Outline each uninfected red blood cell.
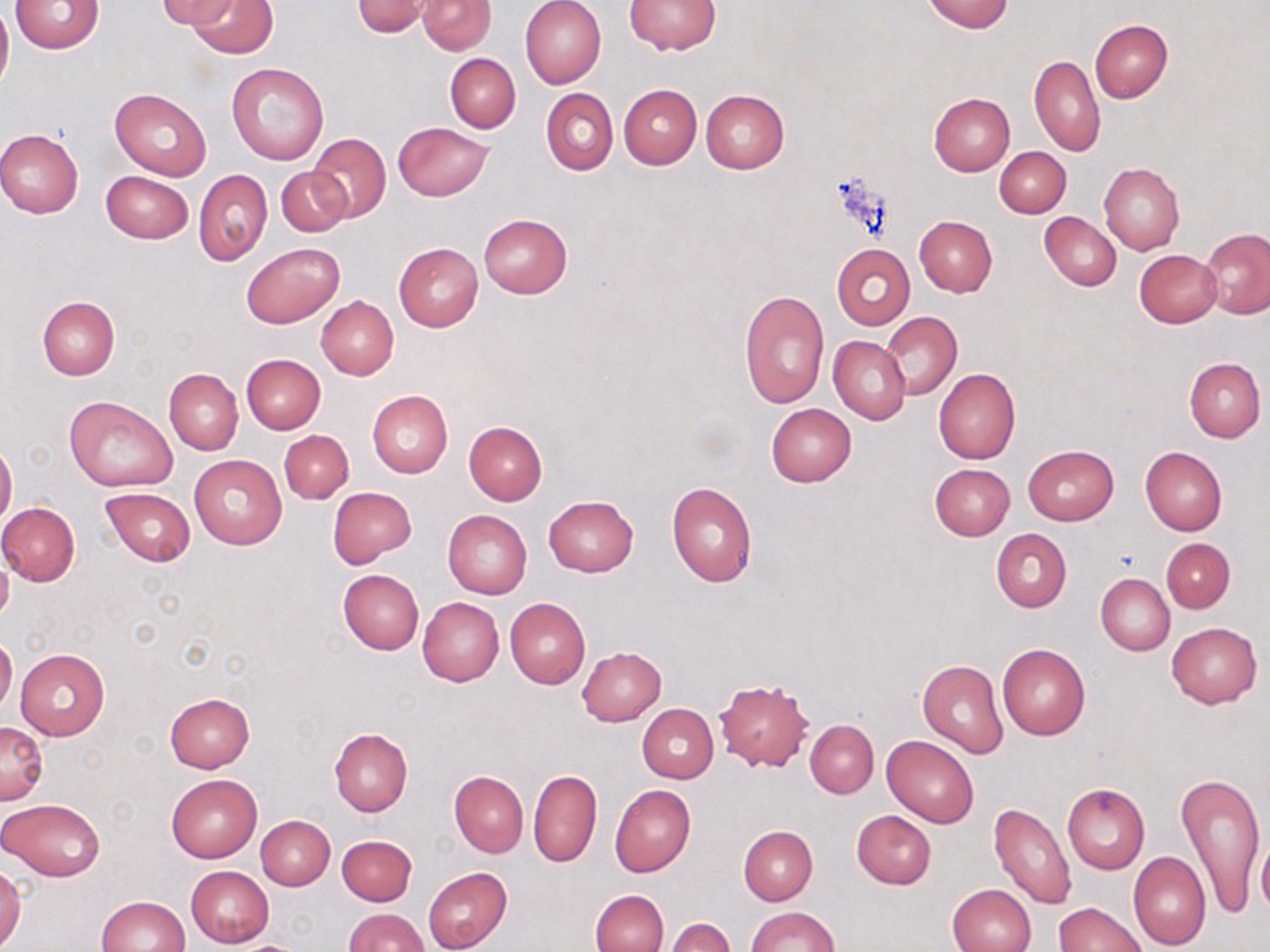
Approximate bounding boxes as (x1,y1)-(x2,y2) corner pairs in pixels.
Uninfected red blood cells: (10,0)-(103,53), (158,0)-(238,29), (188,0)-(278,58), (418,0)-(494,54), (519,0)-(606,89), (922,0)-(1014,33), (0,1)-(13,94), (352,1)-(433,37), (626,1)-(720,54), (1089,19)-(1172,102), (445,53)-(520,132), (1029,55)-(1105,157), (226,62)-(330,165), (619,83)-(701,169), (541,87)-(618,175), (110,88)-(210,180), (701,89)-(789,174), (929,92)-(1015,176), (393,122)-(493,201), (0,130)-(83,219), (306,132)-(391,223), (995,147)-(1070,218), (1099,163)-(1184,254), (277,168)-(349,237), (100,170)-(194,244), (194,170)-(272,264), (1039,212)-(1122,291), (479,213)-(571,297), (915,216)-(996,297), (1201,228)-(1270,318), (242,242)-(344,328), (393,243)-(484,332), (832,244)-(915,328), (1134,250)-(1221,328), (738,289)-(830,410), (317,296)-(398,380), (36,297)-(119,380), (882,310)-(962,401), (828,336)-(911,423), (242,354)-(325,434), (1184,358)-(1265,443), (933,368)-(1020,465), (164,369)-(242,454), (367,390)-(453,477), (65,395)-(177,490), (766,403)-(856,486), (464,422)-(546,504), (279,430)-(353,503), (0,440)-(17,528), (1022,444)-(1119,526), (1140,447)-(1227,536), (189,455)-(286,549), (930,464)-(1014,540), (667,482)-(757,586), (327,486)-(415,566), (101,487)-(195,566), (544,496)-(638,577), (0,502)-(81,585), (443,509)-(532,600), (991,528)-(1072,612), (1162,538)-(1234,613), (0,550)-(13,627), (337,569)-(424,655), (1095,573)-(1175,655), (417,596)-(505,686), (505,597)-(590,689), (1166,622)-(1262,708), (0,636)-(17,713), (997,644)-(1091,740), (577,646)-(666,725), (15,649)-(109,739), (917,659)-(1007,758), (715,680)-(813,771), (164,692)-(254,771), (637,703)-(719,783), (805,719)-(878,798), (0,722)-(48,804), (329,728)-(413,816), (882,735)-(979,828), (528,768)-(601,868), (450,770)-(527,856), (1176,770)-(1266,918), (166,774)-(263,862), (1062,783)-(1149,873), (610,784)-(695,876), (1,797)-(105,881), (987,802)-(1076,910), (851,809)-(936,889), (256,815)-(334,890), (739,826)-(817,905), (1256,832)-(1270,920), (337,835)-(417,905), (1127,850)-(1211,949), (0,866)-(25,949), (186,866)-(274,947), (423,866)-(512,952), (946,884)-(1036,952), (590,889)-(668,952), (95,895)-(190,952), (1054,903)-(1146,952), (746,906)-(837,952), (344,908)-(429,951), (665,917)-(734,952).

slide-level diagnosis = no evidence of blood parasites
modality = light microscopy
magnification = 1000x
stain = May-Grünwald-Giemsa
image size = 1270×952 pixels
preparation = thin blood smear
field of view = single